Locate every malaria parasite.
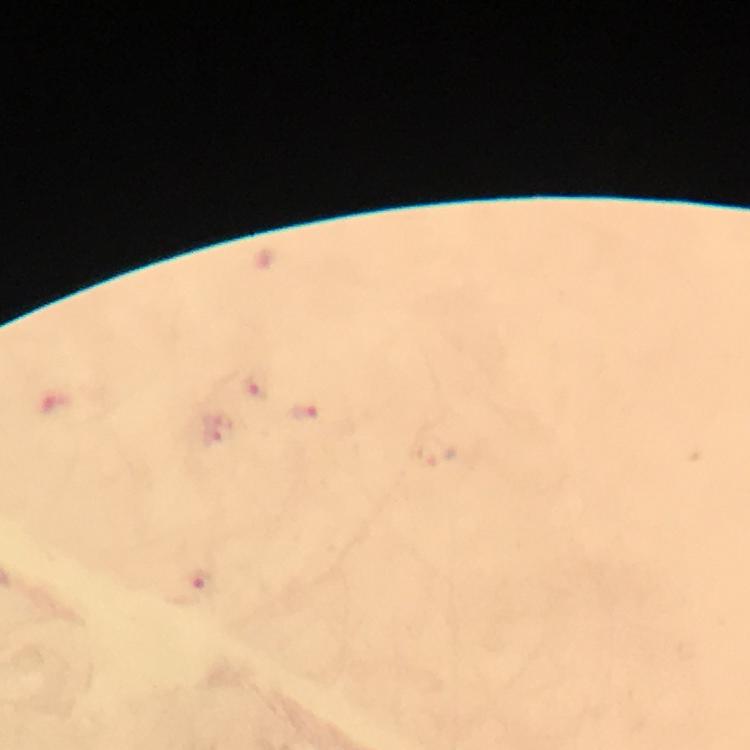

Approximate centers as [x, y] in pixels.
Malaria parasites: [256, 386], [306, 413], [203, 585].

Image is 750×750 pixels. From a diagnostic examination for malaria. Immersion oil applied. A crop from one field of view. Photographed through the microscope with a smartphone camera. At 100x magnification. Thick blood film. Giemsa stain.